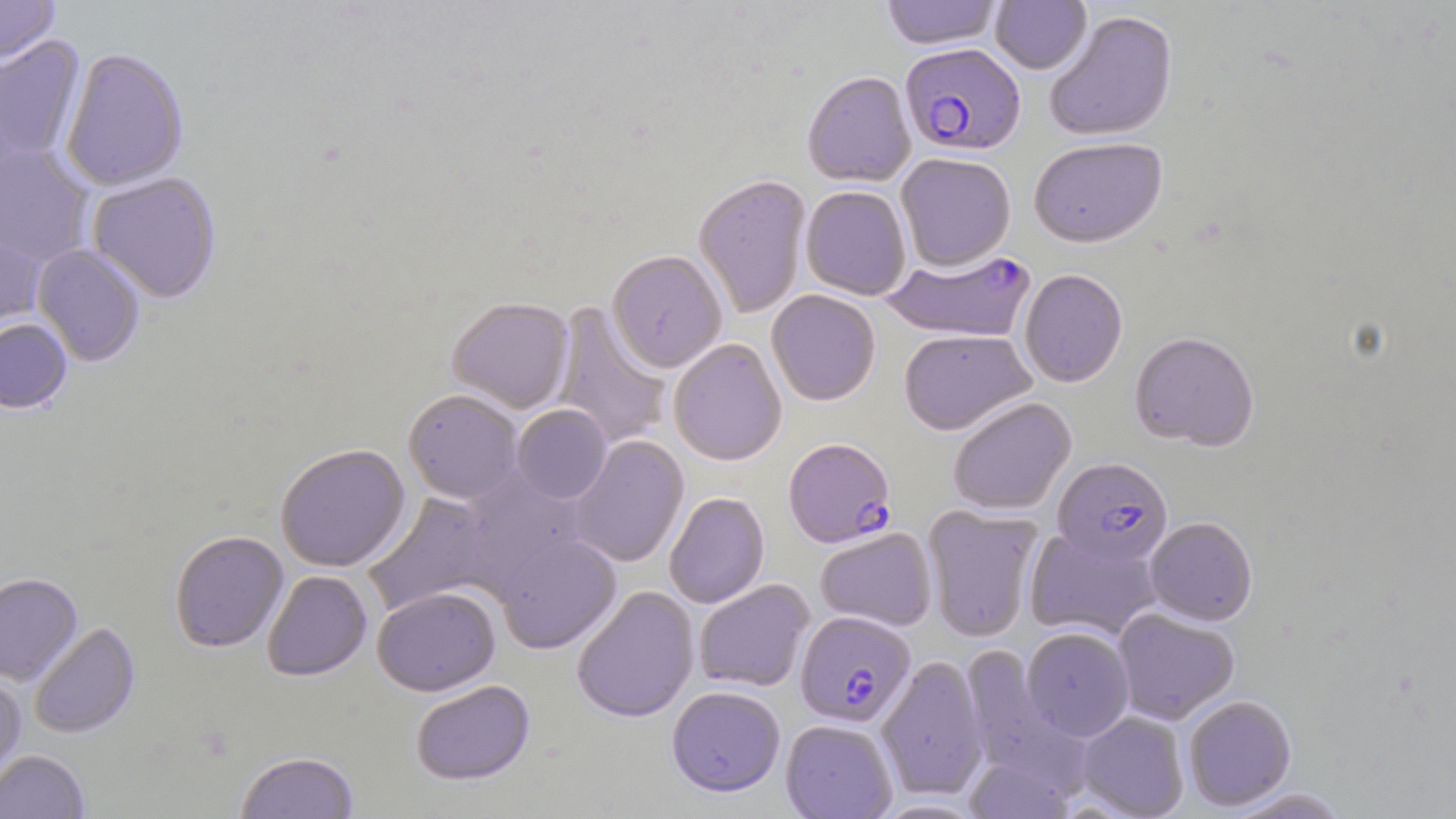

Approximate bounding boxes as (x1, y1, x2, y2) in pixels. Plasmodium falciparum-infected red blood cell locations: (900, 43, 1025, 157), (883, 248, 1035, 343), (783, 437, 896, 548), (1053, 457, 1172, 566), (795, 611, 915, 726). Uninfected red blood cell locations: (0, 0, 60, 66), (881, 0, 1003, 50), (990, 0, 1092, 74), (1044, 10, 1179, 143), (0, 37, 86, 165), (60, 49, 189, 192), (803, 70, 916, 186), (1028, 137, 1167, 248), (0, 144, 95, 268), (896, 152, 1016, 270), (86, 172, 222, 303), (694, 174, 811, 319), (801, 186, 911, 300), (0, 223, 47, 338), (32, 244, 145, 367), (607, 250, 728, 372), (1019, 269, 1127, 387), (767, 290, 881, 406), (447, 297, 574, 413), (552, 304, 672, 450), (0, 318, 73, 415), (899, 328, 1036, 435), (1129, 330, 1259, 451), (668, 338, 787, 465), (403, 389, 524, 504), (948, 397, 1076, 515), (512, 404, 612, 504), (567, 435, 689, 567), (275, 443, 410, 571), (459, 468, 593, 591), (364, 492, 498, 617), (664, 492, 769, 608), (923, 505, 1043, 643), (1145, 516, 1257, 626), (1024, 526, 1163, 642), (815, 527, 936, 631), (170, 530, 289, 652), (495, 533, 621, 653), (262, 570, 372, 680), (0, 573, 82, 685), (693, 579, 814, 692), (372, 586, 499, 695), (571, 586, 699, 722), (1113, 607, 1239, 724), (29, 622, 141, 739), (1022, 626, 1134, 740), (959, 644, 1081, 782), (876, 655, 988, 799), (0, 671, 26, 785), (410, 679, 534, 785), (667, 685, 785, 796), (1183, 694, 1296, 811), (1076, 711, 1189, 818), (781, 719, 897, 819), (0, 750, 91, 818), (234, 751, 360, 818), (963, 754, 1075, 819), (1224, 786, 1351, 818). Slide-level diagnosis: Plasmodium falciparum. Captured at 1000x magnification. Image is 1456×819 pixels. Single field of view. Light microscopy. May-Grünwald-Giemsa-stained preparation. Thin blood film.